Locate and identify every blood parasite.
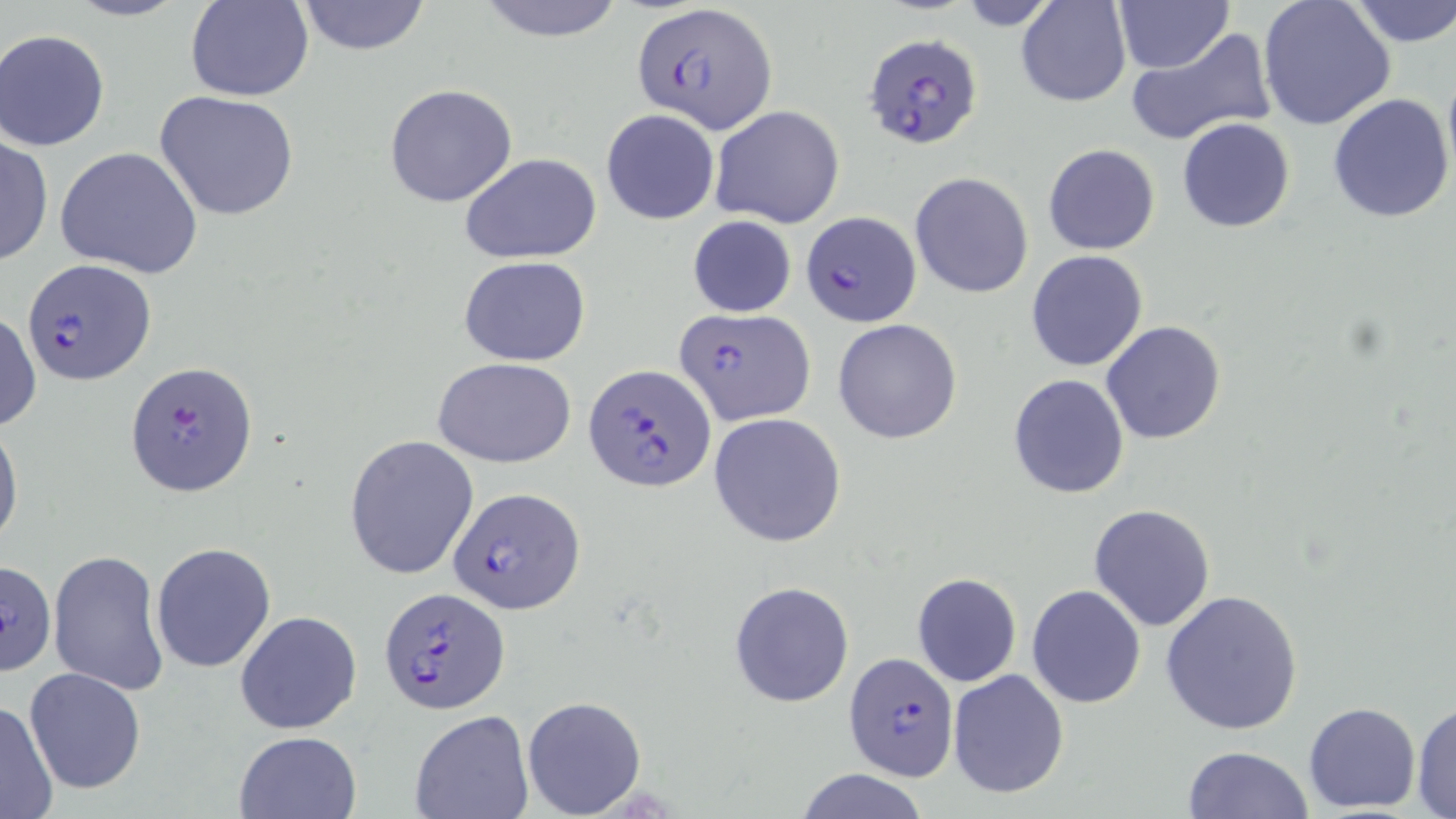

Approximate bounding boxes as named x1/y1/x2/y2 corners in pixels.
Plasmodium falciparum-infected red blood cells: (x1=634, y1=2, x2=777, y2=133), (x1=864, y1=33, x2=984, y2=149), (x1=801, y1=213, x2=920, y2=327), (x1=23, y1=257, x2=156, y2=387), (x1=675, y1=308, x2=815, y2=425), (x1=126, y1=359, x2=258, y2=498), (x1=584, y1=364, x2=714, y2=492), (x1=450, y1=486, x2=587, y2=613), (x1=2, y1=559, x2=58, y2=676), (x1=378, y1=586, x2=511, y2=717), (x1=844, y1=653, x2=958, y2=782).
No Plasmodium ovale, Plasmodium malariae, Plasmodium vivax, Babesia divergens, or Trypanosoma brucei observed.

slide-level diagnosis = Plasmodium falciparum
field of view = single
modality = light microscopy
image size = 1456×819 pixels
magnification = 1000x
stain = May-Grünwald-Giemsa
preparation = thin blood smear
uninfected red blood cell locations = approximate bounding boxes as named x1/y1/x2/y2 corners in pixels: (x1=63, y1=0, x2=191, y2=22), (x1=185, y1=0, x2=313, y2=102), (x1=476, y1=0, x2=626, y2=42), (x1=1016, y1=0, x2=1132, y2=106), (x1=1113, y1=0, x2=1235, y2=73), (x1=1257, y1=0, x2=1396, y2=131), (x1=1346, y1=0, x2=1456, y2=47), (x1=297, y1=1, x2=432, y2=54), (x1=1, y1=28, x2=114, y2=152), (x1=1125, y1=28, x2=1276, y2=147), (x1=1441, y1=62, x2=1456, y2=187), (x1=384, y1=84, x2=517, y2=208), (x1=154, y1=90, x2=301, y2=222), (x1=1328, y1=93, x2=1455, y2=225), (x1=710, y1=104, x2=844, y2=228), (x1=600, y1=108, x2=720, y2=226), (x1=1176, y1=117, x2=1295, y2=233), (x1=0, y1=132, x2=52, y2=267), (x1=1042, y1=143, x2=1160, y2=255), (x1=55, y1=146, x2=204, y2=279), (x1=460, y1=152, x2=602, y2=265), (x1=909, y1=172, x2=1034, y2=298), (x1=688, y1=214, x2=796, y2=317), (x1=1026, y1=250, x2=1148, y2=372), (x1=460, y1=256, x2=591, y2=366), (x1=0, y1=309, x2=41, y2=433), (x1=832, y1=319, x2=963, y2=446), (x1=1100, y1=321, x2=1226, y2=444), (x1=433, y1=356, x2=577, y2=468), (x1=1008, y1=373, x2=1129, y2=499), (x1=707, y1=413, x2=846, y2=547), (x1=0, y1=418, x2=23, y2=553), (x1=344, y1=434, x2=479, y2=580), (x1=1088, y1=503, x2=1216, y2=631), (x1=150, y1=541, x2=276, y2=673), (x1=48, y1=549, x2=169, y2=697), (x1=912, y1=573, x2=1021, y2=687), (x1=728, y1=580, x2=855, y2=707), (x1=1027, y1=584, x2=1146, y2=707), (x1=1161, y1=587, x2=1304, y2=734), (x1=234, y1=610, x2=363, y2=735), (x1=22, y1=667, x2=147, y2=795), (x1=947, y1=669, x2=1069, y2=799), (x1=521, y1=696, x2=647, y2=817), (x1=1, y1=699, x2=59, y2=818), (x1=1410, y1=699, x2=1456, y2=818), (x1=1302, y1=702, x2=1422, y2=813), (x1=409, y1=711, x2=532, y2=819), (x1=234, y1=730, x2=362, y2=819), (x1=1181, y1=744, x2=1314, y2=819), (x1=792, y1=768, x2=932, y2=819)